Assess this cell for malaria.
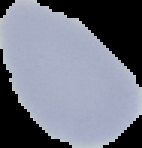

Uninfected.

Summary:
  - Preparation: thin blood film
  - Image type: cell region segmented out of the field of view; surrounding area masked to black
  - Image size: 142×148 pixels